Comment on the morphology of the red blood cells.
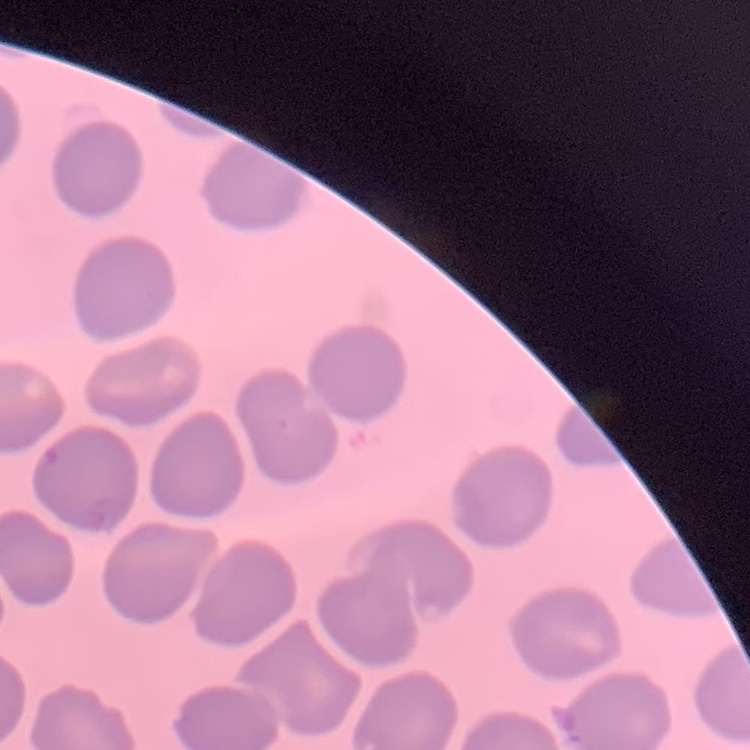

They show no rouleaux formation.

{
  "preparation": "thin blood film",
  "stain": "Field's or Giemsa",
  "image_type": "one tile cut from a larger photomicrograph"
}